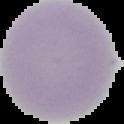

image type = segmented cell region with the area outside set to black
preparation = thin blood film
image size = 124×124 pixels
malaria status = uninfected